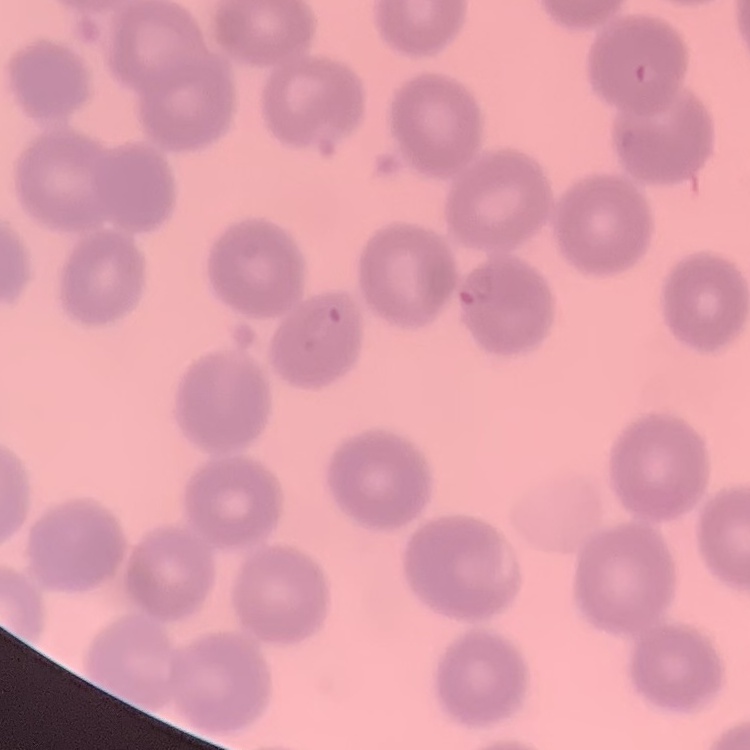

Summary:
  - Erythrocyte morphology: no rouleaux formation
  - Preparation: thin blood smear
  - Stain: Field's or Giemsa
  - Image type: one tile cut from a larger photomicrograph